Point out each leukocyte.
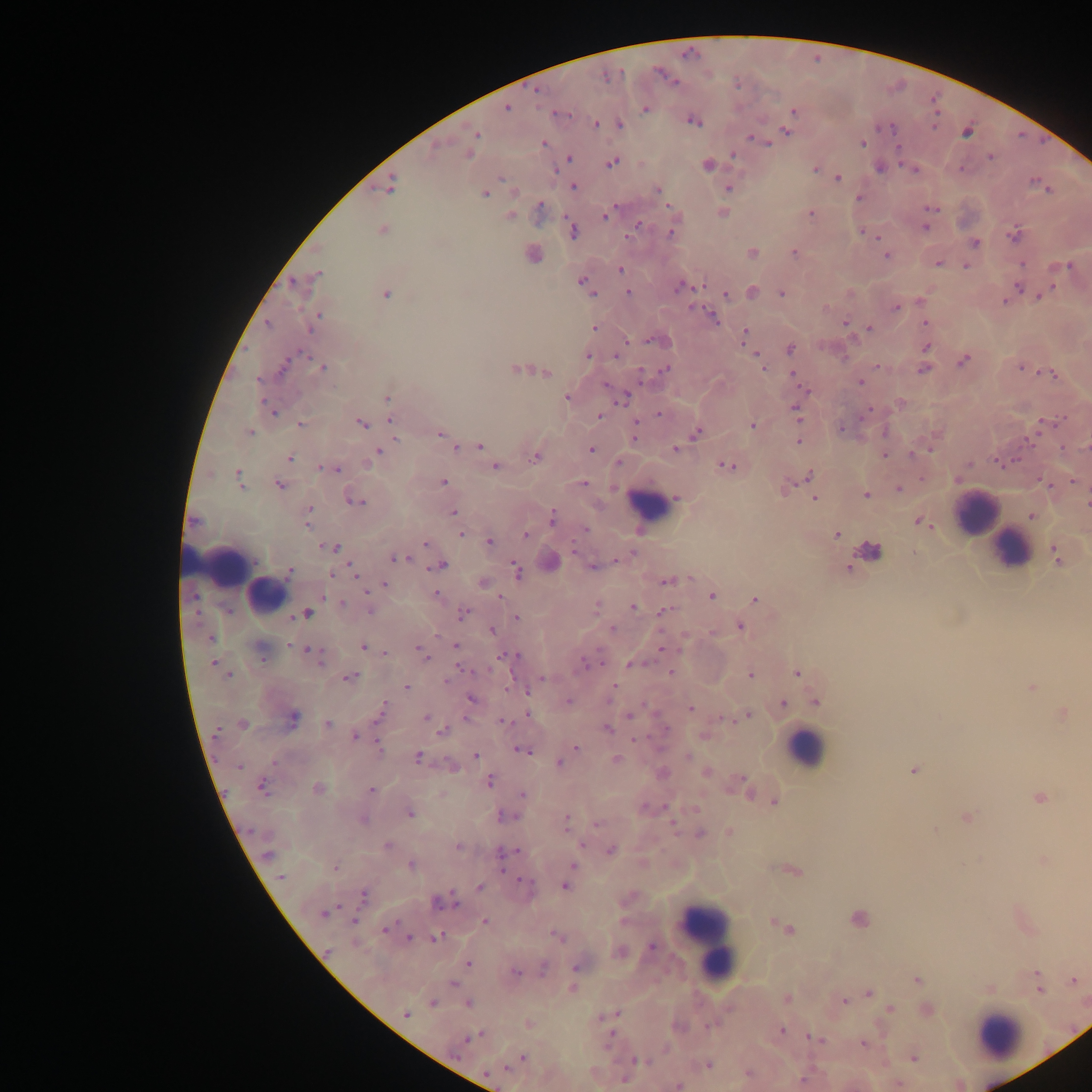
Approximate centers as (x, y) in pixels.
Leukocytes: (655, 502), (977, 515), (1011, 546), (236, 567), (811, 749), (707, 941), (999, 1034).

Summary:
  - Plasmodium parasite locations: (659, 74), (674, 81), (675, 81), (534, 92), (507, 107), (645, 108), (794, 110), (552, 112), (934, 112), (565, 114), (571, 114), (937, 114), (692, 121), (595, 123), (934, 129), (786, 131), (477, 134), (750, 138), (542, 142), (863, 143), (767, 145), (897, 147), (468, 154), (567, 157), (990, 157), (611, 162), (706, 165), (814, 168), (960, 168), (838, 178), (501, 179), (1030, 182), (573, 186), (727, 188), (658, 189), (485, 194), (858, 197), (539, 203), (666, 205), (614, 209), (928, 209), (933, 209), (811, 212), (511, 215), (603, 215), (638, 224), (924, 227), (570, 228), (863, 230), (383, 231), (670, 233), (877, 236), (1011, 236), (627, 237), (975, 242), (795, 252), (752, 253), (887, 254), (938, 263), (1022, 263), (1070, 265), (965, 266), (1052, 267), (620, 269), (622, 273), (318, 275), (581, 281), (585, 286), (1053, 286), (686, 287), (1018, 287), (679, 288), (629, 292), (386, 293), (781, 293), (593, 294), (726, 294), (1039, 296), (1005, 300), (895, 308), (711, 314), (923, 322), (269, 323), (845, 323), (594, 327), (870, 328), (744, 335), (646, 340), (627, 342), (790, 348), (926, 348), (302, 353), (755, 354), (588, 357), (615, 357), (963, 360), (285, 365), (876, 365), (1019, 366), (763, 367), (640, 368), (322, 369), (923, 369), (514, 370), (664, 370), (793, 372), (547, 373), (1054, 374), (257, 380), (862, 381), (605, 385), (806, 389), (626, 397), (566, 398), (386, 399), (263, 400), (797, 407), (869, 408), (658, 413), (275, 414), (599, 416), (390, 419), (637, 421), (861, 421), (1044, 421), (1057, 421), (360, 423), (299, 425), (365, 426), (754, 426), (841, 428), (250, 432), (1037, 432), (440, 433), (697, 433), (635, 438), (395, 439), (799, 441), (1026, 443), (480, 446), (675, 447), (455, 448), (1063, 448), (591, 449), (931, 449), (378, 451), (884, 454), (910, 454), (534, 456), (291, 458), (1015, 459), (995, 462), (971, 464), (726, 466), (495, 467), (318, 468), (337, 469), (236, 472), (810, 475), (921, 477), (958, 478), (1074, 481), (444, 482), (584, 483), (278, 484), (241, 486), (1051, 486), (898, 488), (867, 495), (677, 497), (814, 498), (356, 501), (362, 502), (310, 509), (454, 514), (552, 516), (919, 519), (309, 526), (931, 526), (585, 529), (836, 534), (460, 535), (525, 536), (487, 541), (425, 542), (322, 546), (336, 548), (575, 550), (631, 552), (393, 558), (408, 558), (616, 561), (443, 565), (593, 566), (351, 567), (431, 568), (516, 569), (290, 572), (330, 575), (357, 575), (666, 582), (384, 583), (367, 592), (437, 592), (191, 596), (500, 596), (323, 598), (714, 598), (755, 599), (344, 601), (632, 607), (370, 610), (661, 611), (308, 612), (461, 612), (296, 616), (515, 617), (740, 625), (613, 629), (493, 631), (712, 631), (438, 636), (211, 639), (289, 644), (363, 647), (418, 647), (455, 647), (307, 649), (314, 649), (661, 650), (385, 652), (422, 652), (500, 655), (518, 655), (426, 660), (262, 661), (213, 662), (583, 663), (320, 664), (603, 664), (629, 665), (459, 667), (465, 670), (671, 672), (797, 672), (229, 674), (750, 674), (354, 676), (348, 677), (542, 677), (447, 679), (614, 685), (406, 687), (1032, 687), (508, 690), (528, 692), (471, 699), (568, 700), (783, 703), (691, 707), (526, 714), (1063, 714), (380, 715), (630, 715), (747, 715), (294, 716), (426, 718), (725, 718), (719, 719), (500, 721), (328, 724), (218, 729), (610, 729), (441, 731), (355, 736), (632, 740), (378, 743), (577, 746), (519, 750), (525, 753), (475, 756), (687, 756), (417, 757), (617, 759), (274, 762), (560, 763), (239, 768), (489, 782), (736, 782), (261, 786), (371, 788), (751, 793), (522, 795), (1039, 798), (775, 801), (500, 814), (412, 815), (507, 815), (567, 816), (966, 819), (597, 823), (671, 824), (249, 830), (567, 830), (935, 830), (388, 844), (581, 844), (457, 846), (517, 850), (611, 850), (266, 855), (1042, 860), (412, 865), (573, 865), (335, 867), (501, 869), (281, 878), (520, 880), (564, 885), (480, 886), (454, 891), (364, 894), (437, 903), (339, 904), (454, 904), (322, 915), (398, 920), (485, 921), (354, 922), (387, 928), (385, 931), (409, 937), (435, 937), (650, 946), (327, 951), (468, 964), (574, 968), (518, 973), (543, 973), (918, 979), (1073, 980), (453, 983), (575, 987), (867, 992), (843, 1001), (433, 1002), (467, 1004), (890, 1008), (616, 1013), (406, 1014), (602, 1017), (706, 1026), (781, 1030), (810, 1036), (466, 1041), (863, 1043), (523, 1057), (914, 1057), (635, 1060), (707, 1066), (506, 1067), (747, 1074), (900, 1083), (677, 1086)
  - Image size: 1092×1092 pixels
  - Country: Ghana
  - Capture: mobile-phone photograph through a microscope
  - Preparation: thick blood film
  - Field of view: single